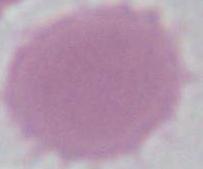
modality: micrograph
magnification: 1000x
identification: red blood cell